Report the malaria status of this cell.
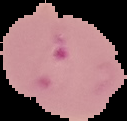

Parasitized.

Summary:
  - Preparation: thin blood smear
  - Image type: cell region segmented out of the field of view; surrounding area masked to black
  - Image size: 127×121 pixels